Assess this cell for malaria.
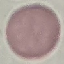

It is uninfected.

{
  "preparation": "thin blood smear",
  "stain": "Giemsa",
  "image_type": "cell patch, automatically extracted from a larger field of view and resized to 64 × 64 pixels",
  "capture": "smartphone through the microscope eyepiece"
}